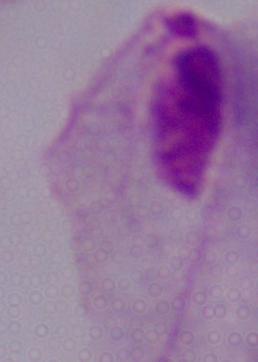
Summary:
  - Identification: trichomonad
  - Modality: photomicrograph
  - Magnification: 1000x